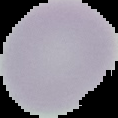

{
  "image_type": "segmented cell region with the area outside set to black",
  "preparation": "thin blood film",
  "image_size": "118×118 pixels",
  "result": "no Plasmodium parasites detected"
}